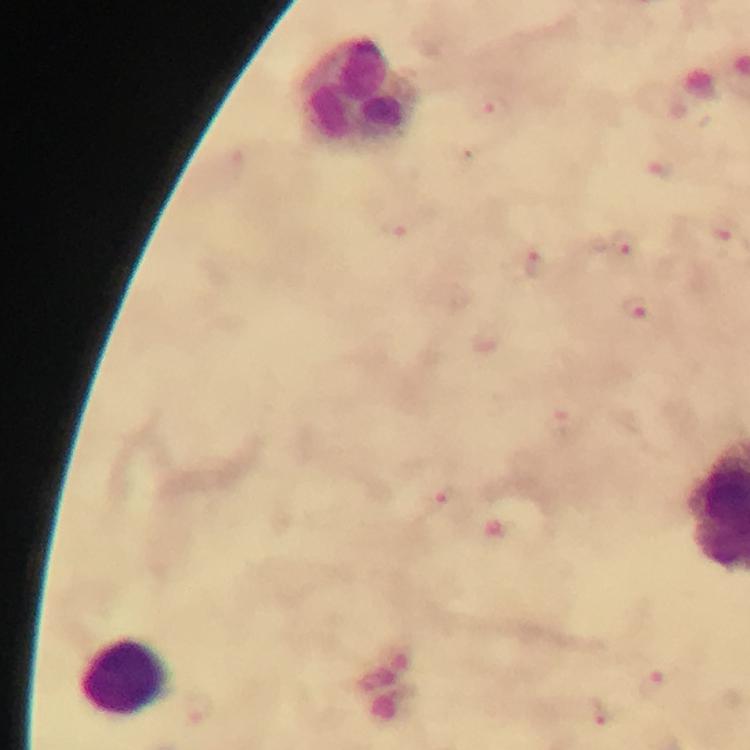
Approximate object centers, in pixels from the top-left corner. Malaria parasite locations: (x=491, y=109), (x=620, y=249), (x=538, y=267), (x=641, y=309), (x=564, y=421), (x=441, y=504), (x=651, y=682), (x=608, y=713). Leukocyte locations: (x=362, y=91), (x=124, y=677). Immersion oil applied. Giemsa stain. Image is 750×750 pixels. Thick blood film. From a diagnostic examination for malaria. 100x magnification. Cropped region of a single field of view. Smartphone photograph taken through a microscope.